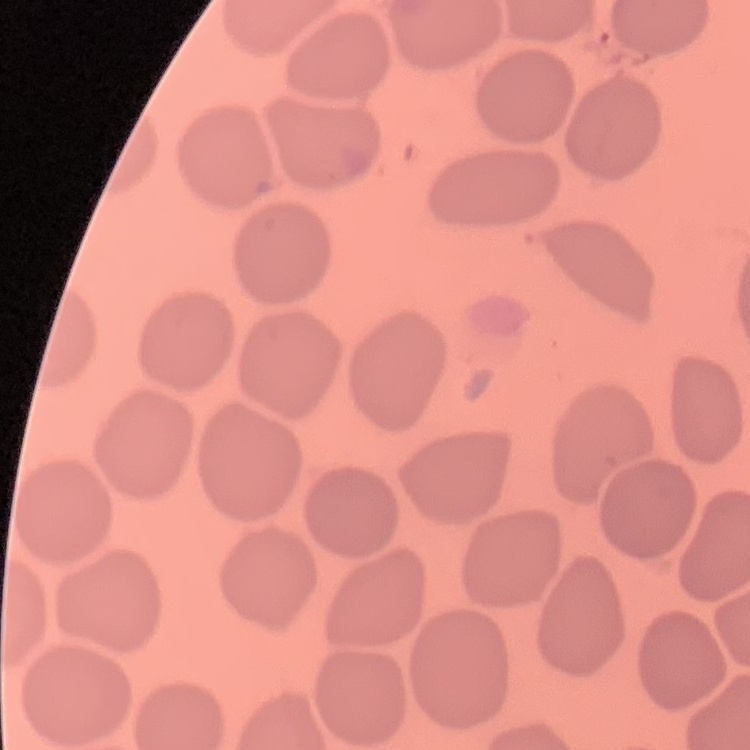
red blood cell morphology = no rouleaux formation
image type = square crop of a larger photomicrograph
preparation = thin peripheral smear
stain = Field's or Giemsa